Identify the parasite.
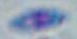
This is Toxoplasma gondii.

modality = photomicrograph
magnification = 1000x